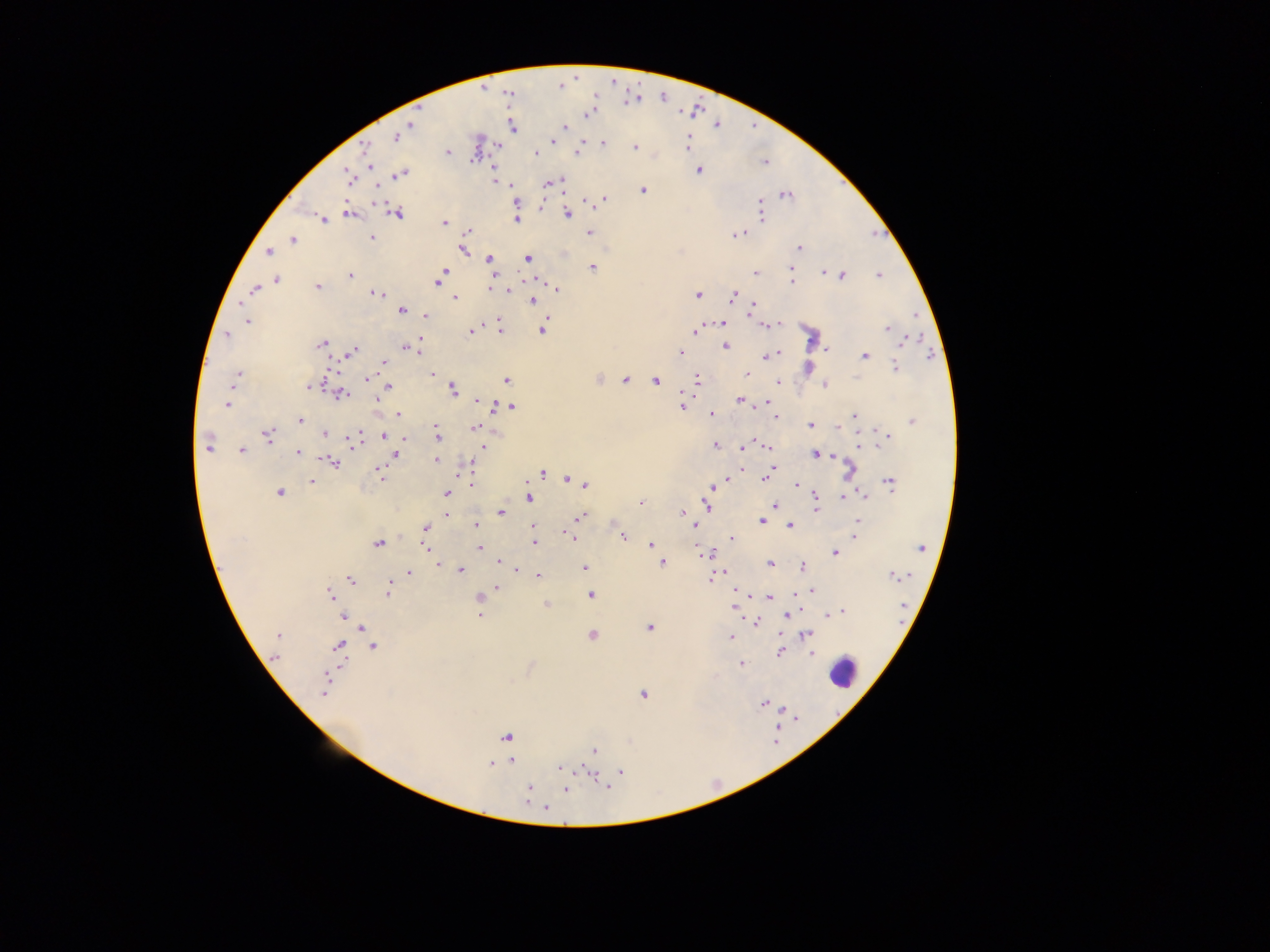
image_size: 1270×952 pixels
capture: mobile-phone photograph through a microscope
country: Ghana
field_of_view: single
preparation: thick blood film
plasmodium_parasite_locations: 'approximate centers as {x, y} in pixels: {560, 84}, {588, 112}, {565, 126}, {408, 127}, {512, 127}, {396, 136}, {553, 141}, {686, 142}, {602, 143}, {497, 144}, {635, 146}, {365, 152}, {577, 152}, {447, 153}, {534, 154}, {369, 161}, {764, 163}, {699, 170}, {399, 173}, {493, 175}, {349, 176}, {494, 180}, {560, 180}, {545, 183}, {550, 183}, {511, 185}, {514, 189}, {642, 190}, {785, 194}, {603, 198}, {586, 202}, {540, 206}, {760, 207}, {348, 213}, {396, 213}, {568, 214}, {760, 214}, {517, 219}, {322, 220}, {444, 222}, {589, 232}, {739, 233}, {467, 234}, {371, 238}, {292, 239}, {799, 248}, {462, 249}, {268, 252}, {489, 259}, {528, 259}, {591, 267}, {790, 268}, {822, 272}, {755, 273}, {350, 275}, {841, 275}, {879, 275}, {440, 276}, {276, 279}, {790, 280}, {318, 287}, {254, 288}, {514, 288}, {488, 289}, {508, 289}, {556, 289}, {378, 294}, {697, 294}, {734, 296}, {454, 297}, {533, 300}, {753, 306}, {401, 310}, {426, 314}, {247, 321}, {723, 323}, {781, 324}, {764, 325}, {886, 327}, {542, 328}, {500, 329}, {470, 330}, {694, 330}, {227, 334}, {911, 339}, {906, 340}, {321, 344}, {724, 345}, {407, 347}, {826, 348}, {419, 349}, {350, 352}, {680, 353}, {779, 353}, {864, 355}, {772, 356}, {384, 362}, {894, 365}, {432, 374}, {747, 374}, {236, 375}, {367, 378}, {598, 379}, {625, 379}, {506, 380}, {654, 380}, {696, 380}, {777, 382}, {824, 385}, {310, 386}, {387, 386}, {452, 390}, {340, 393}, {682, 396}, {376, 399}, {477, 400}, {740, 400}, {227, 404}, {506, 405}, {682, 406}, {497, 407}, {511, 407}, {398, 414}, {711, 414}, {854, 416}, {773, 417}, {300, 420}, {912, 422}, {435, 423}, {810, 424}, {836, 426}, {473, 428}, {436, 429}, {324, 433}, {358, 433}, {267, 435}, {384, 435}, {886, 435}, {403, 438}, {438, 438}, {354, 440}, {879, 442}, {715, 445}, {207, 446}, {483, 446}, {768, 446}, {742, 447}, {241, 450}, {298, 452}, {394, 454}, {814, 454}, {831, 455}, {436, 460}, {332, 462}, {470, 467}, {771, 467}, {742, 469}, {849, 471}, {379, 473}, {541, 473}, {767, 475}, {381, 478}, {765, 478}, {567, 479}, {312, 480}, {726, 480}, {889, 482}, {585, 484}, {472, 485}, {710, 486}, {797, 486}, {279, 491}, {446, 493}, {814, 494}, {864, 494}, {528, 497}, {844, 497}, {639, 502}, {705, 505}, {774, 505}, {815, 511}, {501, 512}, {682, 512}, {447, 513}, {580, 516}, {762, 521}, {857, 521}, {475, 525}, {790, 525}, {533, 526}, {694, 526}, {425, 527}, {854, 533}, {569, 536}, {621, 536}, {732, 538}, {377, 542}, {534, 542}, {650, 544}, {695, 546}, {426, 547}, {479, 547}, {920, 548}, {834, 552}, {498, 561}, {661, 562}, {440, 565}, {770, 565}, {584, 566}, {803, 567}, {460, 568}, {516, 569}, {409, 573}, {537, 575}, {893, 575}, {710, 578}, {350, 579}, {498, 587}, {390, 590}, {734, 590}, {812, 591}, {330, 594}, {590, 594}, {478, 597}, {769, 597}, {545, 605}, {735, 608}, {842, 610}, {789, 612}, {830, 613}, {478, 614}, {785, 614}, {343, 616}, {756, 622}, {649, 627}, {361, 628}, {278, 635}, {592, 635}, {806, 635}, {731, 638}, {277, 643}, {373, 646}, {338, 648}, {780, 650}, {811, 654}, {275, 656}, {740, 663}, {325, 686}, {642, 694}, {764, 703}, {505, 738}, {594, 750}, {511, 760}, {490, 764}, {559, 767}, {619, 770}, {588, 772}, {605, 783}, {528, 788}, {565, 789}, {544, 807}'
leukocyte_locations: 'approximate centers as {x, y} in pixels: {843, 672}'